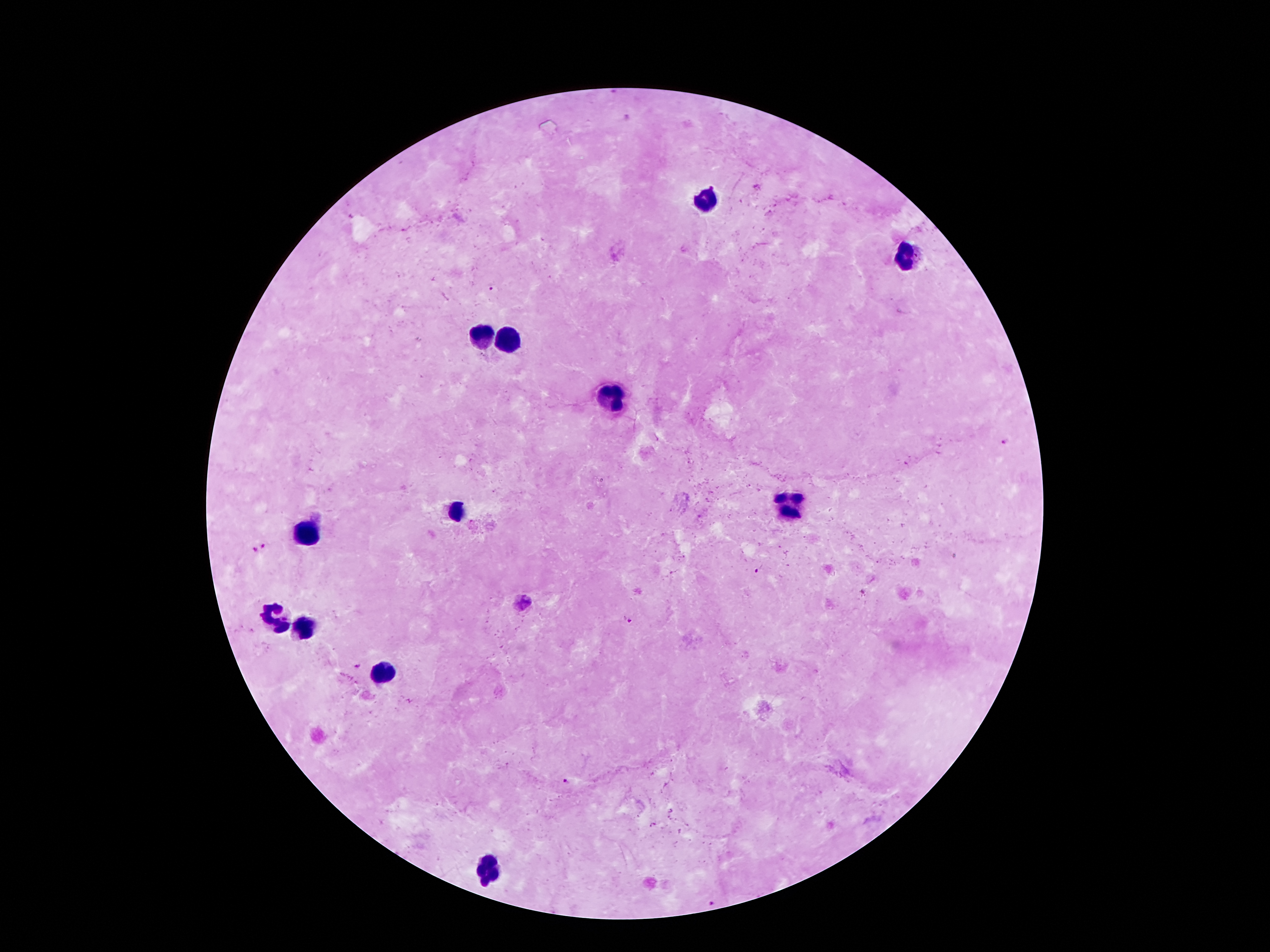

{
  "magnification": "100x",
  "capture": "smartphone through the microscope eyepiece",
  "stain": "Giemsa",
  "preparation": "thick peripheral-blood smear",
  "field_of_view": "single",
  "image_size": "1270×952 pixels",
  "patient_malaria_status": "positive for Plasmodium falciparum",
  "malaria_parasite_locations": "approximate centers as [x, y] in pixels: [490, 288], [1003, 442], [266, 547], [253, 550], [756, 571], [862, 591], [522, 603], [629, 621], [359, 667], [566, 782], [715, 901]",
  "leukocyte_locations": "approximate centers as [x, y] in pixels: [707, 197], [903, 256], [481, 338], [506, 342], [617, 397], [794, 506], [460, 512], [306, 533], [271, 617], [304, 628], [384, 669], [491, 868]"
}